Identify the cell.
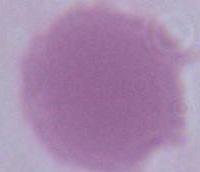

This is an erythrocyte.

1000x magnification. Photomicrograph.